Describe the morphology of the red blood cells.
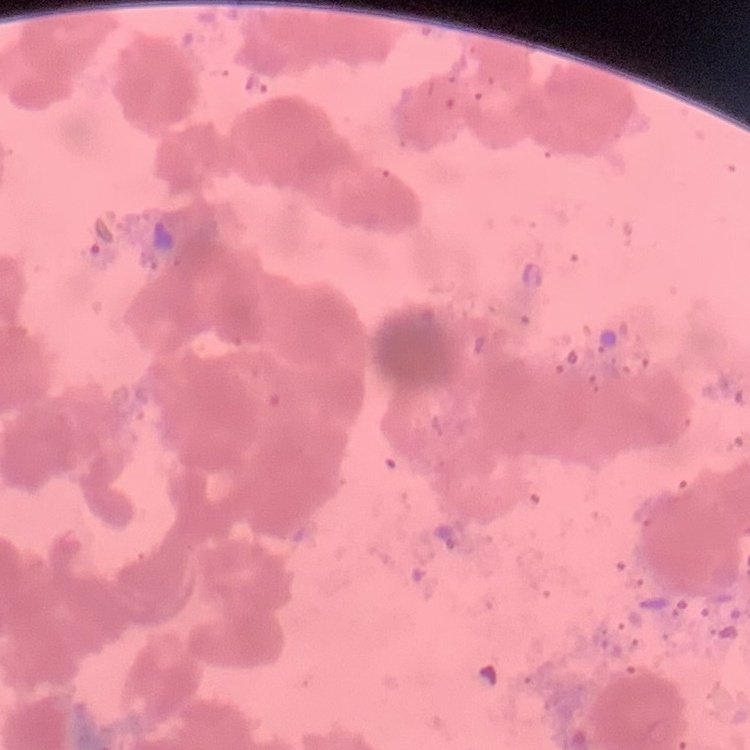
Rouleaux formation.

{
  "stain": "Field's or Giemsa",
  "image_type": "square crop of a larger photomicrograph",
  "preparation": "thin peripheral smear"
}